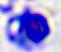
Summary:
  - Identification: leukocyte
  - Magnification: 400x
  - Modality: photomicrograph